Classify this cell by malaria status.
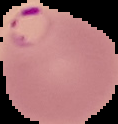

It is parasitized.

Summary:
  - Image type: segmented cell region on a black background
  - Image size: 118×124 pixels
  - Preparation: thin blood smear